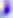
Summary:
  - Magnification: 400x
  - Identification: Toxoplasma gondii
  - Modality: photomicrograph